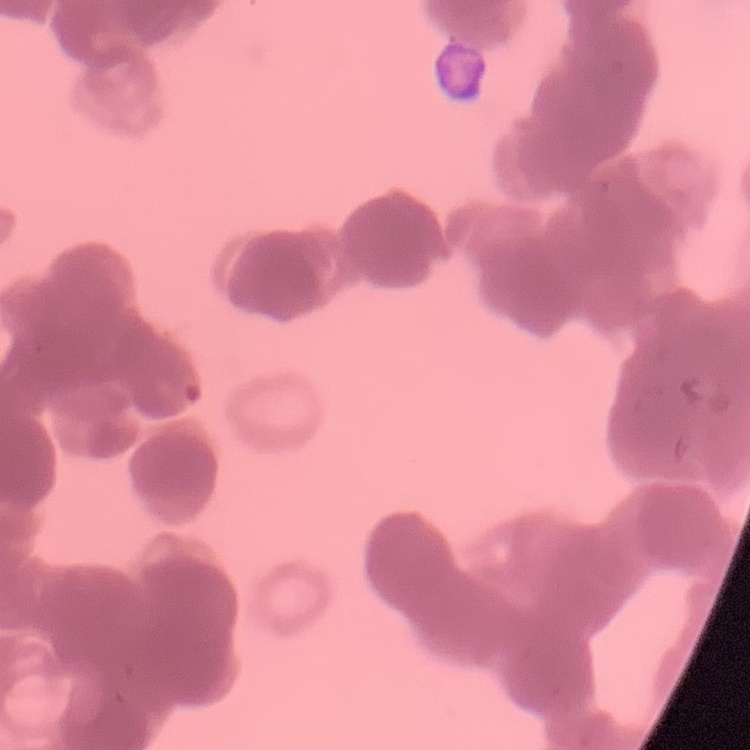

red blood cell morphology = rouleaux formation
preparation = thin blood film
stain = Field's or Giemsa
image type = square crop of a larger photomicrograph